Locate every leukocyte (white blood cell).
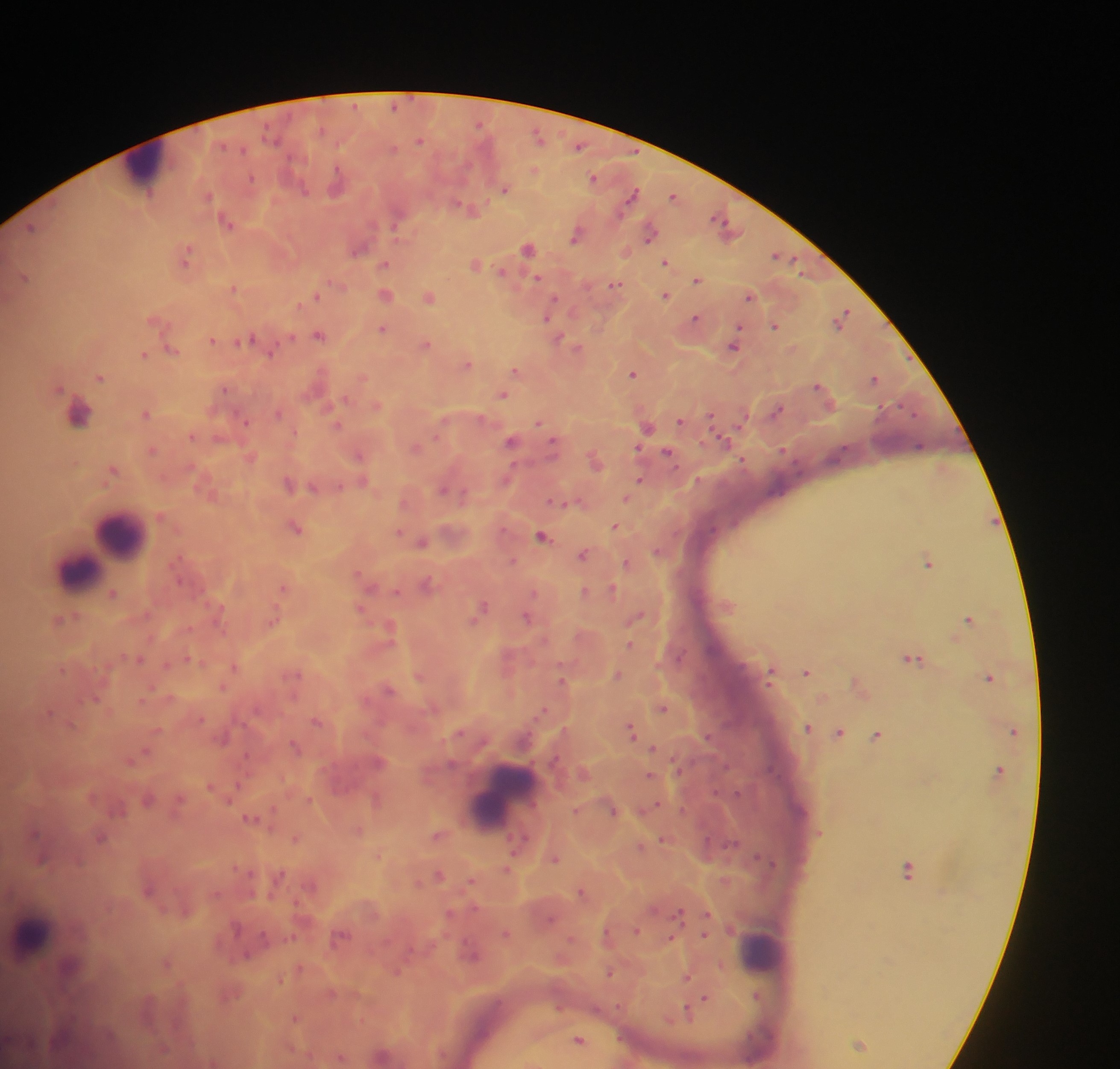

Approximate centers as (x, y) in pixels.
Leukocytes: (147, 170), (120, 536), (97, 558), (78, 569), (505, 798), (33, 933), (762, 949).

image size = 1120×1069 pixels
country = Ghana
field of view = single
preparation = thick blood smear
capture = mobile-phone photograph through a microscope
Plasmodium parasite locations = approximate centers as (x, y) in pixels: (355, 105), (394, 105), (480, 123), (271, 134), (539, 136), (419, 140), (579, 144), (243, 148), (392, 148), (535, 169), (593, 176), (252, 177), (336, 181), (303, 187), (504, 188), (633, 193), (208, 194), (673, 195), (460, 204), (719, 218), (228, 223), (31, 226), (650, 233), (574, 235), (359, 247), (528, 247), (187, 253), (776, 254), (665, 261), (384, 263), (475, 264), (502, 270), (25, 276), (538, 276), (697, 279), (615, 283), (233, 286), (387, 294), (315, 295), (666, 295), (749, 295), (429, 297), (546, 315), (696, 317), (842, 317), (776, 325), (383, 328), (738, 330), (319, 335), (292, 336), (212, 338), (558, 338), (246, 339), (426, 343), (735, 344), (578, 347), (172, 349), (272, 352), (144, 353), (468, 364), (516, 369), (632, 373), (100, 376), (874, 378), (818, 385), (225, 387), (59, 388), (503, 394), (377, 405), (777, 409), (77, 412), (146, 412), (278, 412), (711, 415), (481, 417), (244, 420), (538, 421), (680, 421), (337, 424), (647, 426), (191, 435), (218, 438), (724, 439), (511, 440), (553, 441), (919, 445), (416, 447), (783, 448), (153, 449), (638, 449), (667, 452), (358, 454), (743, 459), (595, 461), (113, 470), (640, 479), (363, 480), (288, 483), (341, 485), (314, 487), (442, 488), (463, 497), (626, 497), (555, 500), (615, 525), (296, 527), (398, 532), (542, 535), (421, 541), (657, 551), (583, 553), (513, 560), (928, 561), (626, 562), (358, 572), (426, 582), (283, 587), (585, 590), (612, 590), (397, 591), (112, 592), (533, 592), (482, 606), (361, 609), (478, 613), (636, 616), (526, 617), (969, 618), (274, 619), (60, 620), (473, 620), (390, 628), (630, 644), (139, 658), (191, 658), (913, 658), (167, 663), (233, 666), (806, 671), (617, 674), (770, 676), (988, 676), (562, 678), (222, 686), (388, 688), (96, 698), (664, 708), (544, 709), (48, 712), (201, 718), (316, 721), (807, 727), (631, 729), (839, 731), (877, 734), (707, 736), (224, 738), (294, 744), (652, 748), (144, 752), (379, 761), (649, 774), (210, 784), (147, 799), (377, 799), (656, 803), (614, 811), (251, 817), (34, 832), (438, 835), (100, 837), (295, 838), (663, 838), (520, 840), (555, 858), (41, 859), (507, 868), (908, 870), (440, 874), (470, 881), (148, 890), (580, 891), (475, 908), (449, 913), (678, 913), (706, 914), (236, 927), (636, 930), (506, 933), (704, 933), (340, 936), (671, 938), (246, 954), (472, 955), (166, 962), (397, 970), (609, 972), (686, 976), (279, 979), (704, 999), (697, 1004), (689, 1010), (295, 1018), (579, 1039), (860, 1043)